State which parasite is depicted.
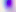

This is Toxoplasma gondii.

modality = photomicrograph
magnification = 400x